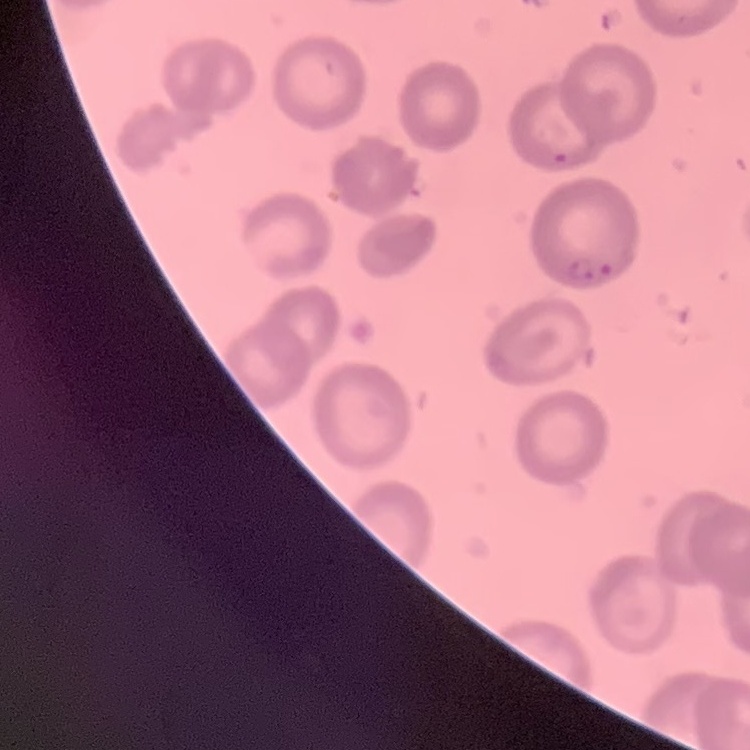

red blood cell morphology = no rouleaux formation
stain = Field's or Giemsa
preparation = thin blood film
image type = square crop of a larger photomicrograph